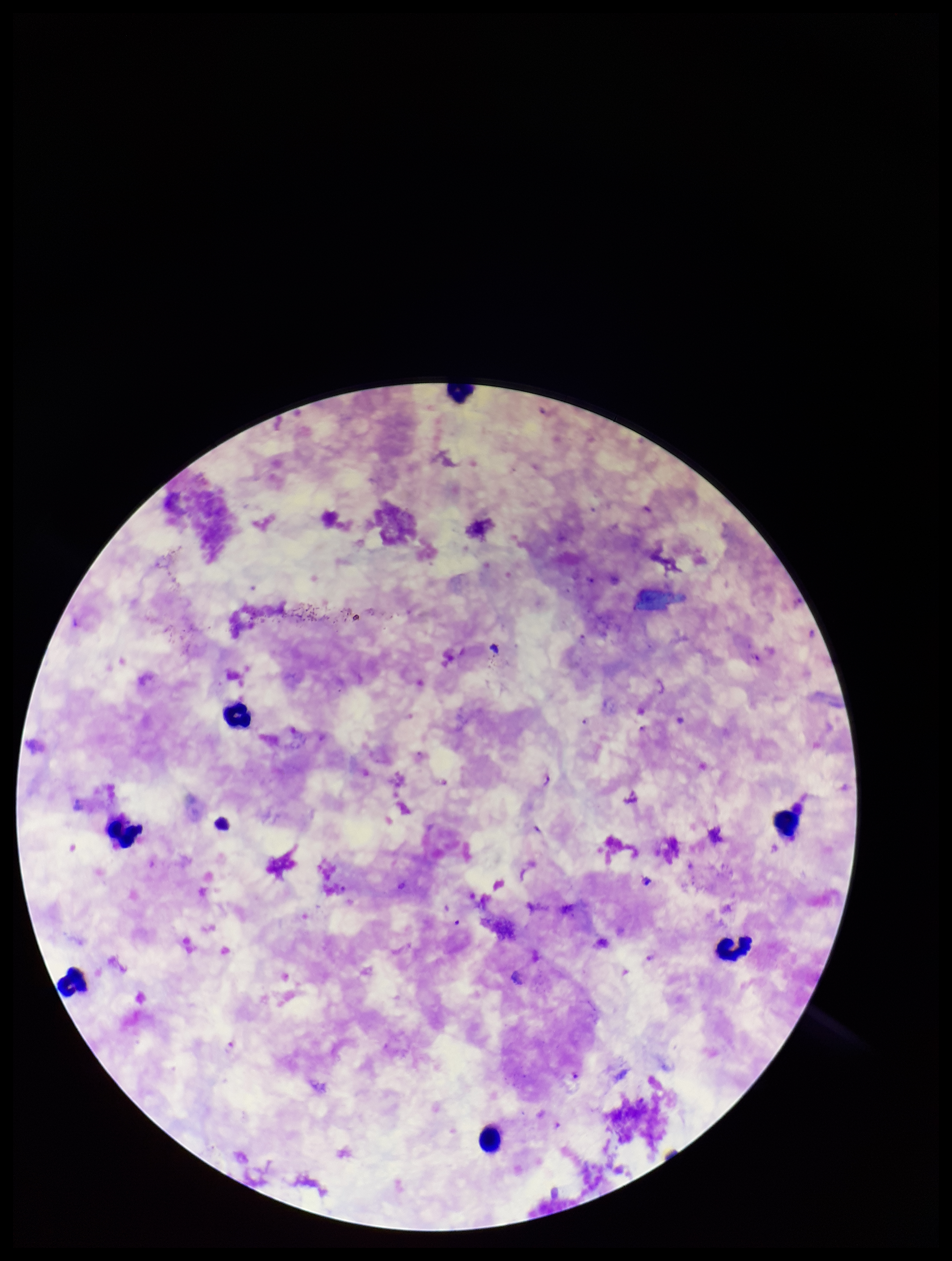
parasite count = 3
capture = smartphone photograph through the microscope eyepiece
species reported for this patient = Plasmodium falciparum
image size = 952×1261 pixels
preparation = thick blood smear
Plasmodium parasites = seen
field of view = single
leukocyte count = 7
patient malaria status = infected
stain = Giemsa